Give the extent of all Plasmodium vivax-infected red blood cells.
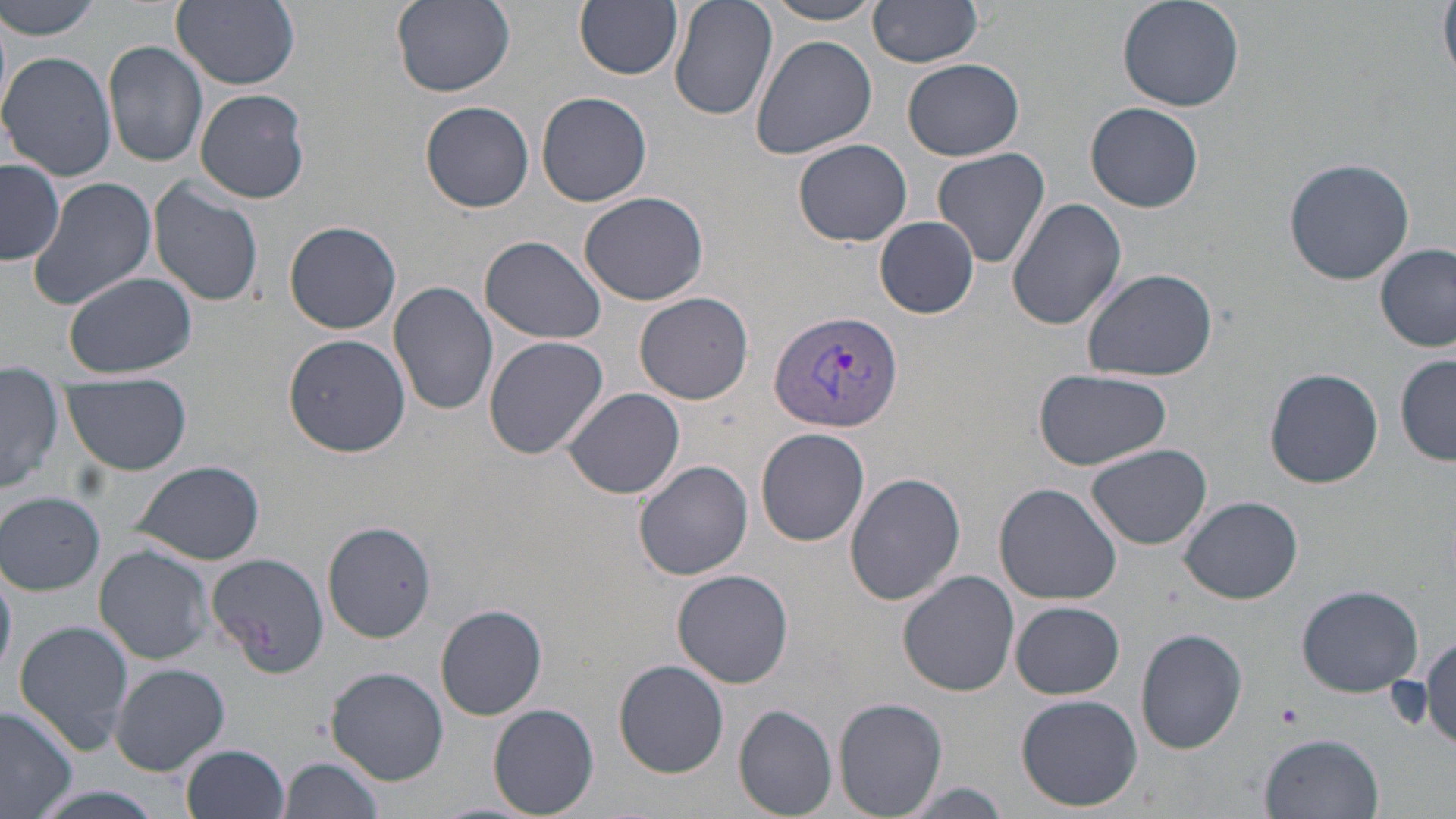
Approximate bounding boxes as (x1, y1, x2, y2) in pixels.
Plasmodium vivax-infected red blood cells: (768, 311, 902, 434).

slide-level diagnosis = Plasmodium vivax
magnification = 1000x
preparation = thin blood smear
uninfected red blood cell locations = approximate bounding boxes as (x1, y1, x2, y2) in pixels: (2, 0, 106, 40), (392, 0, 516, 96), (575, 0, 684, 80), (668, 0, 778, 121), (868, 0, 988, 68), (1115, 0, 1244, 111), (1439, 0, 1456, 79), (174, 1, 301, 89), (760, 1, 886, 25), (1, 11, 14, 120), (749, 33, 877, 160), (105, 40, 210, 168), (2, 54, 117, 180), (903, 58, 1024, 160), (195, 88, 310, 204), (535, 91, 652, 206), (419, 100, 535, 212), (1087, 102, 1203, 212), (793, 139, 913, 245), (932, 147, 1051, 271), (1282, 157, 1418, 285), (1, 159, 64, 266), (28, 176, 156, 310), (149, 179, 264, 308), (580, 192, 712, 307), (1006, 198, 1128, 331), (875, 216, 980, 318), (284, 219, 402, 333), (481, 234, 606, 345), (1376, 243, 1454, 351), (1081, 267, 1219, 382), (64, 272, 196, 378), (389, 280, 499, 417), (635, 293, 754, 406), (284, 333, 410, 458), (483, 335, 610, 461), (1396, 354, 1456, 466), (1264, 368, 1383, 488), (1033, 369, 1170, 471), (63, 373, 192, 475), (2, 374, 61, 496), (561, 388, 686, 499), (755, 427, 871, 547), (1087, 442, 1212, 551), (633, 459, 754, 581), (133, 460, 266, 565), (845, 471, 967, 606), (994, 482, 1124, 606), (1, 491, 105, 594), (1179, 495, 1303, 604), (321, 519, 438, 644), (95, 545, 217, 664), (205, 550, 332, 676), (0, 554, 17, 684), (672, 568, 794, 688), (898, 570, 1019, 696), (1295, 583, 1423, 697), (1009, 601, 1125, 699), (435, 605, 548, 720), (13, 619, 134, 757), (1136, 628, 1248, 754), (1421, 634, 1456, 750), (614, 660, 729, 777), (110, 663, 230, 775), (326, 667, 449, 786), (1016, 694, 1143, 811), (834, 698, 948, 817), (488, 704, 599, 818), (734, 704, 838, 816), (0, 705, 79, 818), (1261, 734, 1383, 818), (182, 744, 290, 819), (279, 755, 386, 819), (894, 780, 1015, 819)
stain = May-Grünwald-Giemsa
platelet locations = approximate bounding boxes as (x1, y1, x2, y2) in pixels: (1275, 701, 1304, 731)
field of view = one of a larger specimen
modality = light microscopy
image size = 1456×819 pixels